Outline each blood parasite and name the species.
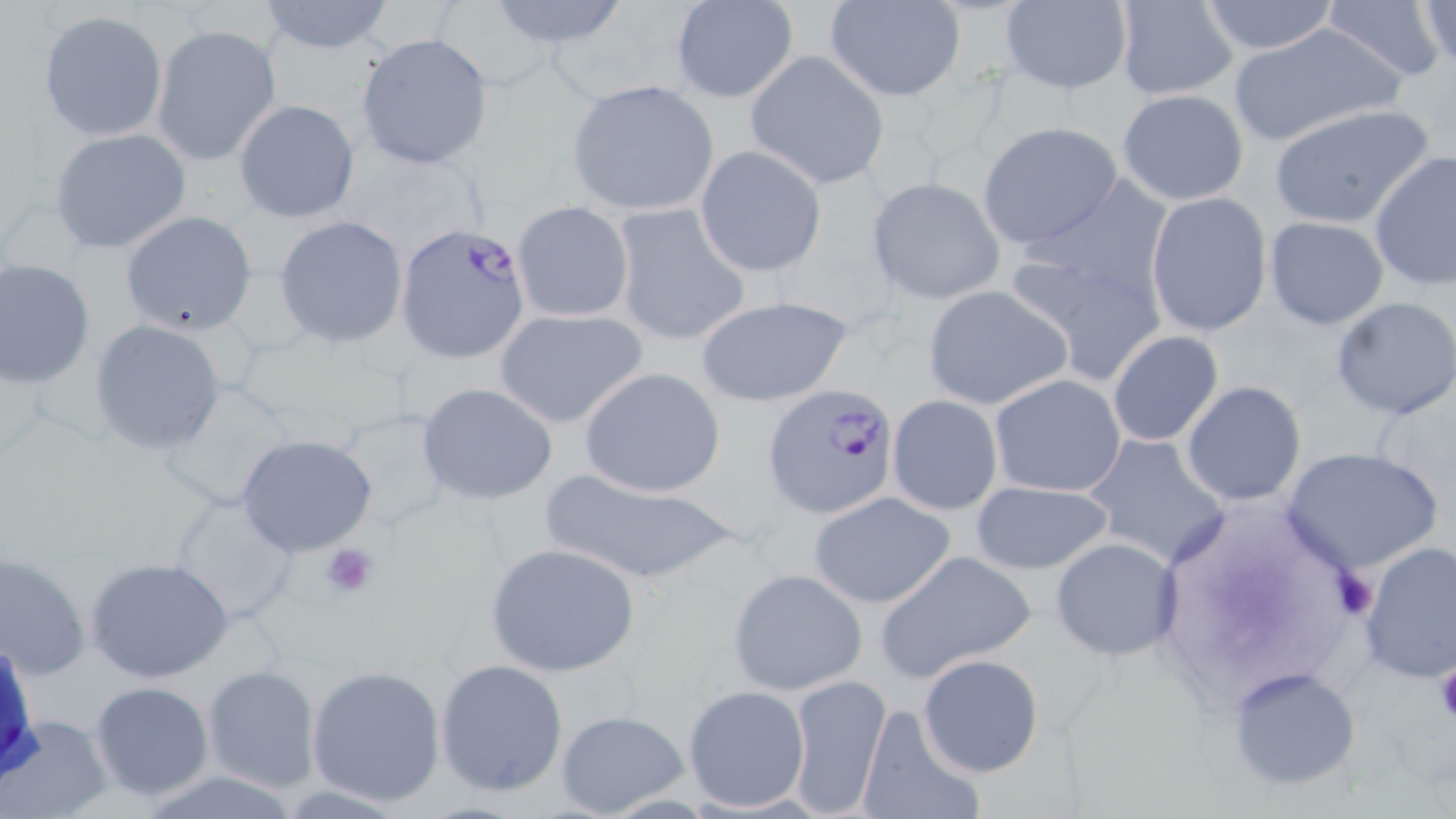
Approximate bounding boxes as (x1, y1, x2, y2) in pixels.
Plasmodium falciparum-infected red blood cells: (395, 221, 533, 364), (762, 384, 899, 518).
No Plasmodium ovale, Plasmodium malariae, Plasmodium vivax, Babesia divergens, or Trypanosoma brucei observed.

slide_level_diagnosis: Plasmodium falciparum
platelet_locations: 'approximate bounding boxes as (x1, y1, x2, y2) in pixels: (320, 542, 380, 599), (1334, 567, 1378, 619), (1433, 667, 1456, 726)'
preparation: thin blood film
uninfected_red_blood_cell_locations: 'approximate bounding boxes as (x1, y1, x2, y2) in pixels: (254, 0, 397, 54), (480, 0, 637, 52), (668, 0, 799, 104), (825, 0, 966, 101), (996, 0, 1133, 95), (1321, 0, 1452, 84), (1112, 1, 1240, 100), (1196, 1, 1341, 56), (1415, 1, 1454, 72), (38, 9, 169, 142), (1228, 22, 1407, 148), (151, 23, 282, 166), (354, 33, 493, 170), (744, 50, 889, 190), (565, 80, 720, 215), (1116, 89, 1249, 206), (232, 98, 360, 225), (1268, 103, 1434, 230), (977, 121, 1123, 251), (47, 128, 193, 253), (695, 145, 826, 278), (1369, 151, 1456, 291), (866, 176, 1006, 306), (1145, 192, 1272, 337), (511, 200, 635, 323), (611, 203, 749, 347), (119, 209, 258, 336), (274, 216, 408, 348), (1263, 216, 1390, 330), (1001, 244, 1170, 385), (0, 258, 97, 389), (922, 286, 1071, 410), (695, 295, 853, 408), (1331, 297, 1456, 421), (493, 308, 648, 429), (89, 319, 227, 455), (1106, 331, 1223, 446), (579, 367, 726, 499), (990, 373, 1126, 497), (153, 379, 306, 511), (1181, 381, 1307, 505), (416, 382, 559, 505), (887, 394, 1002, 516), (330, 408, 452, 533), (236, 433, 379, 558), (1082, 434, 1231, 567), (1282, 447, 1445, 577), (538, 466, 739, 585), (969, 480, 1115, 574), (809, 491, 956, 609), (167, 494, 302, 624), (1050, 536, 1182, 661), (1356, 540, 1455, 684), (486, 543, 640, 676), (875, 550, 1036, 682), (1, 551, 91, 681), (87, 557, 234, 685), (726, 567, 868, 697), (917, 653, 1044, 777), (435, 658, 568, 796), (202, 663, 322, 792), (305, 663, 447, 805), (1229, 665, 1363, 791), (787, 672, 891, 818), (89, 681, 216, 802), (683, 684, 811, 812), (854, 701, 986, 819), (555, 709, 690, 819), (3, 713, 112, 818)'
image_size: 1456×819 pixels
modality: optical microscopy
magnification: 1000x
stain: May-Grünwald-Giemsa
field_of_view: one of a larger specimen